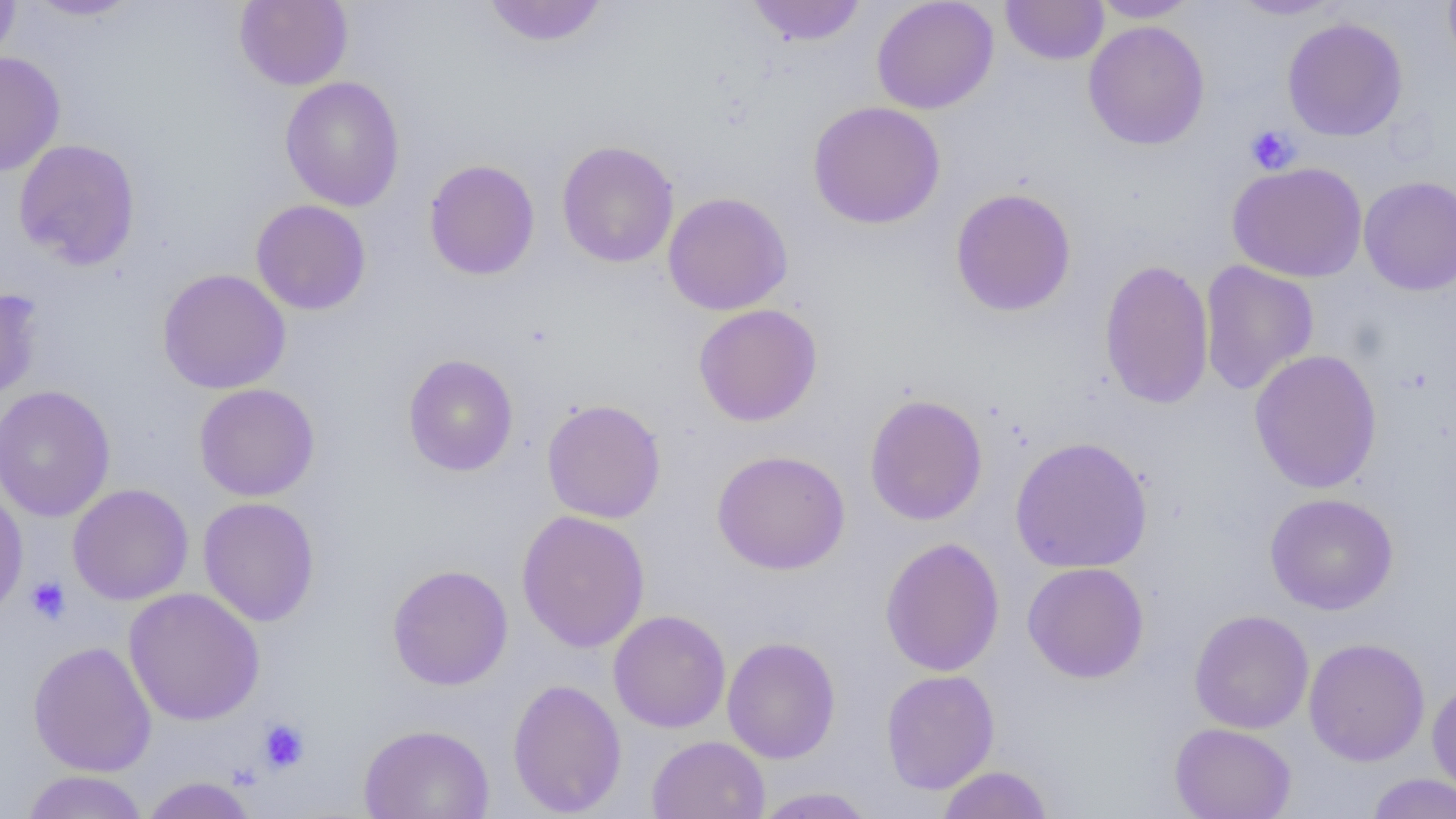

Summary:
  - Coordinate format: approximate bounding boxes as named x1/y1/x2/y2 corners in pixels
  - Platelet locations: (x1=1245, y1=124, x2=1300, y2=174), (x1=26, y1=576, x2=71, y2=625), (x1=257, y1=719, x2=310, y2=773)
  - Uninfected red blood cell locations: (x1=0, y1=0, x2=20, y2=65), (x1=23, y1=0, x2=141, y2=20), (x1=234, y1=0, x2=353, y2=90), (x1=481, y1=0, x2=610, y2=47), (x1=745, y1=0, x2=867, y2=46), (x1=870, y1=0, x2=999, y2=114), (x1=1000, y1=0, x2=1109, y2=65), (x1=1090, y1=0, x2=1201, y2=22), (x1=1227, y1=0, x2=1345, y2=20), (x1=1443, y1=0, x2=1456, y2=76), (x1=1282, y1=16, x2=1408, y2=141), (x1=1083, y1=20, x2=1210, y2=150), (x1=0, y1=51, x2=66, y2=177), (x1=279, y1=76, x2=405, y2=212), (x1=808, y1=101, x2=946, y2=229), (x1=13, y1=138, x2=141, y2=270), (x1=556, y1=140, x2=679, y2=268), (x1=424, y1=159, x2=540, y2=280), (x1=1227, y1=161, x2=1367, y2=283), (x1=1358, y1=175, x2=1456, y2=296), (x1=950, y1=187, x2=1077, y2=317), (x1=662, y1=192, x2=793, y2=315), (x1=251, y1=199, x2=371, y2=315), (x1=1099, y1=258, x2=1214, y2=410), (x1=1199, y1=260, x2=1319, y2=396), (x1=157, y1=268, x2=291, y2=394), (x1=0, y1=287, x2=42, y2=402), (x1=693, y1=304, x2=823, y2=427), (x1=1248, y1=349, x2=1383, y2=493), (x1=403, y1=354, x2=519, y2=476), (x1=194, y1=383, x2=320, y2=502), (x1=0, y1=385, x2=116, y2=522), (x1=864, y1=393, x2=988, y2=526), (x1=541, y1=399, x2=666, y2=523), (x1=1010, y1=436, x2=1153, y2=573), (x1=711, y1=449, x2=851, y2=575), (x1=67, y1=483, x2=194, y2=605), (x1=0, y1=486, x2=28, y2=619), (x1=1264, y1=492, x2=1399, y2=615), (x1=197, y1=497, x2=321, y2=626), (x1=516, y1=509, x2=650, y2=653), (x1=880, y1=537, x2=1005, y2=677), (x1=1022, y1=562, x2=1149, y2=683), (x1=386, y1=563, x2=513, y2=691), (x1=123, y1=587, x2=265, y2=726), (x1=1189, y1=609, x2=1314, y2=734), (x1=608, y1=610, x2=731, y2=733), (x1=722, y1=636, x2=841, y2=764), (x1=1303, y1=637, x2=1430, y2=766), (x1=28, y1=640, x2=157, y2=777), (x1=881, y1=669, x2=1000, y2=794), (x1=507, y1=678, x2=627, y2=817), (x1=1427, y1=678, x2=1456, y2=798), (x1=1169, y1=723, x2=1297, y2=819), (x1=358, y1=724, x2=495, y2=819), (x1=646, y1=735, x2=770, y2=818), (x1=936, y1=765, x2=1054, y2=819), (x1=21, y1=770, x2=148, y2=818), (x1=1365, y1=773, x2=1456, y2=818), (x1=139, y1=776, x2=258, y2=818), (x1=751, y1=786, x2=879, y2=818)
  - Slide-level diagnosis: negative for blood parasites
  - Magnification: 1000x
  - Modality: optical microscopy
  - Field of view: single
  - Image size: 1456×819 pixels
  - Preparation: thin blood smear